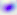

identification = Toxoplasma gondii
modality = photomicrograph
magnification = 400x